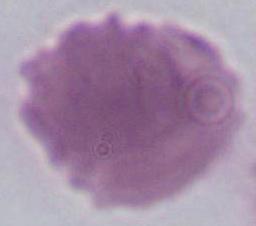

Micrograph. A red blood cell is shown. Captured at 1000x magnification.